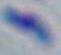
Toxoplasma gondii is shown. Captured at 1000x magnification. Micrograph.